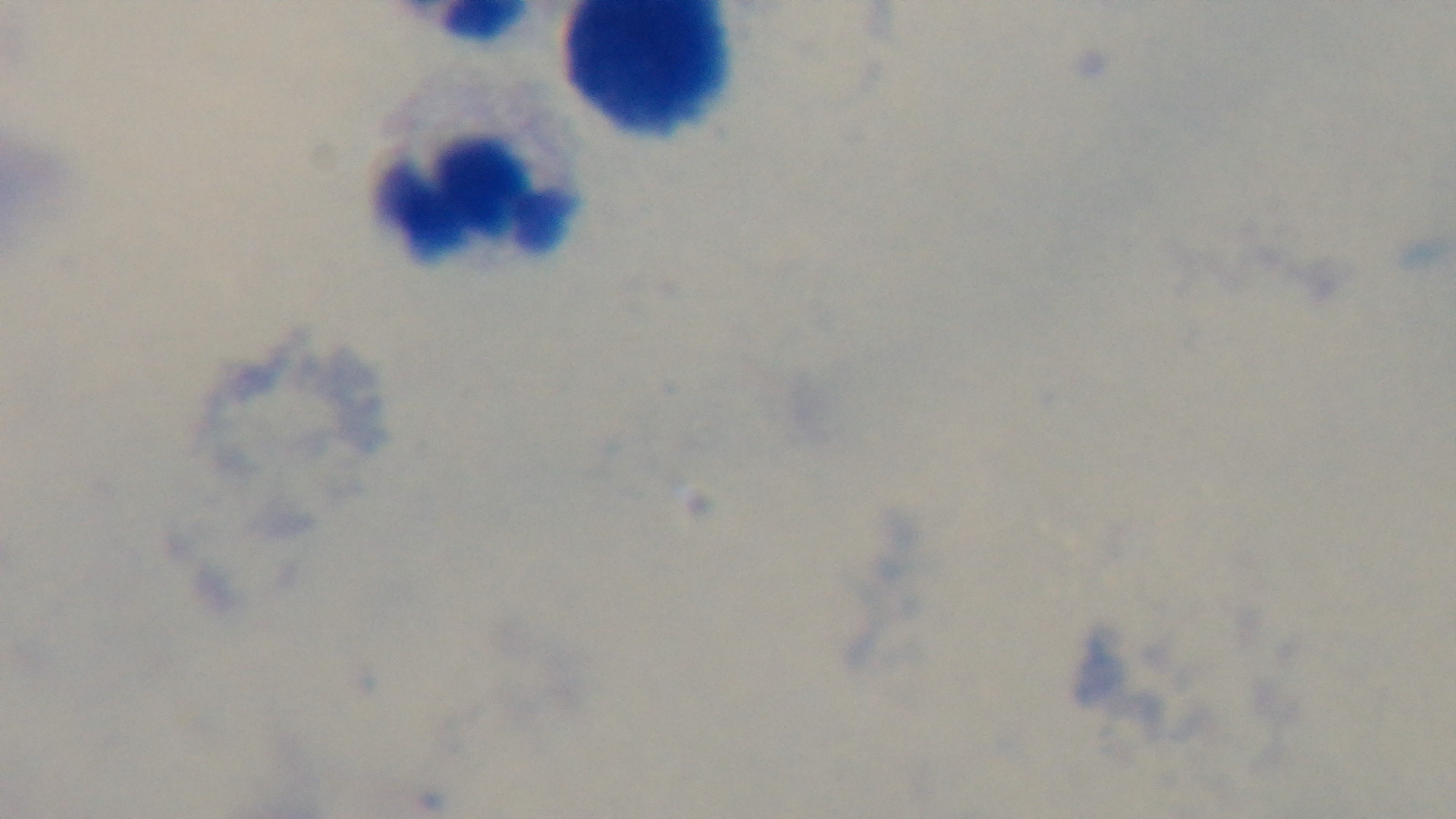
Summary:
  - Field of view: one from the slide
  - Preparation: thick blood film
  - Capture: mounted 4K digital camera
  - Objective: 100x oil immersion
  - Modality: light microscopy
  - Stain: Giemsa
  - Malaria status: uninfected